Comment on the morphology of the erythrocytes.
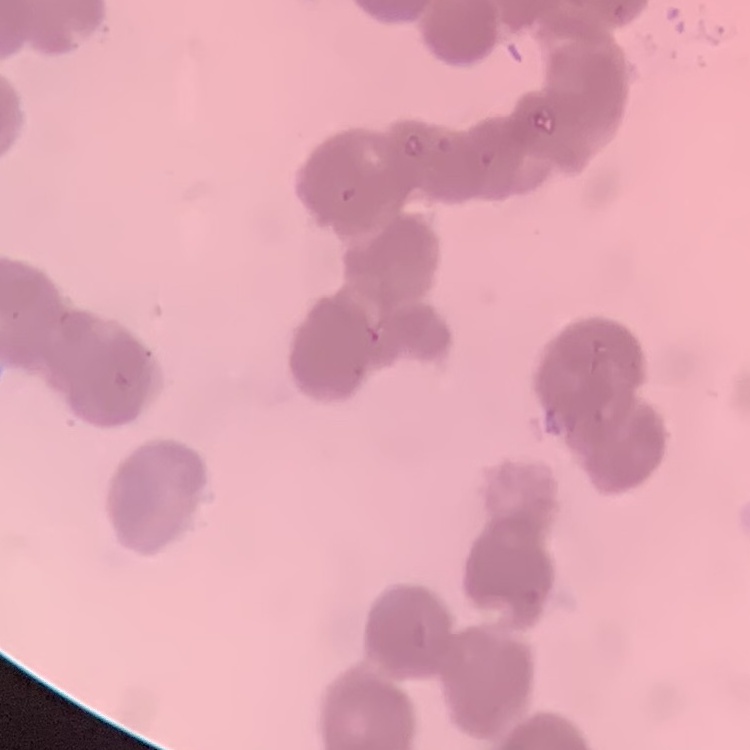
They show rouleaux formation.

Summary:
  - Stain: Field's or Giemsa
  - Image type: one tile cut from a larger photomicrograph
  - Preparation: thin blood smear